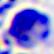

Summary:
  - Identification: white blood cell
  - Modality: micrograph
  - Magnification: 400x